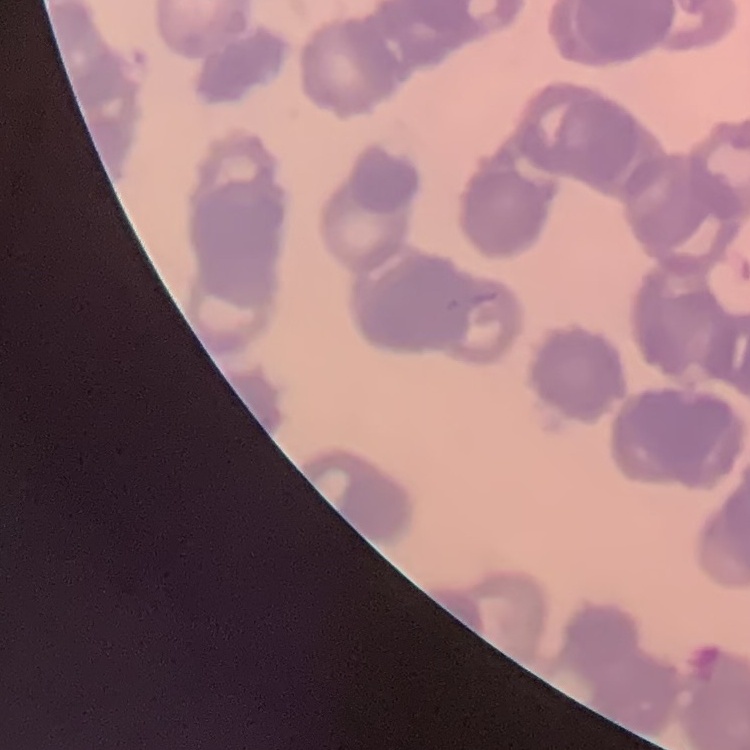
The erythrocytes exhibit rouleaux formation. Thin blood film. Square crop of a larger photomicrograph. Field's or Giemsa stain.